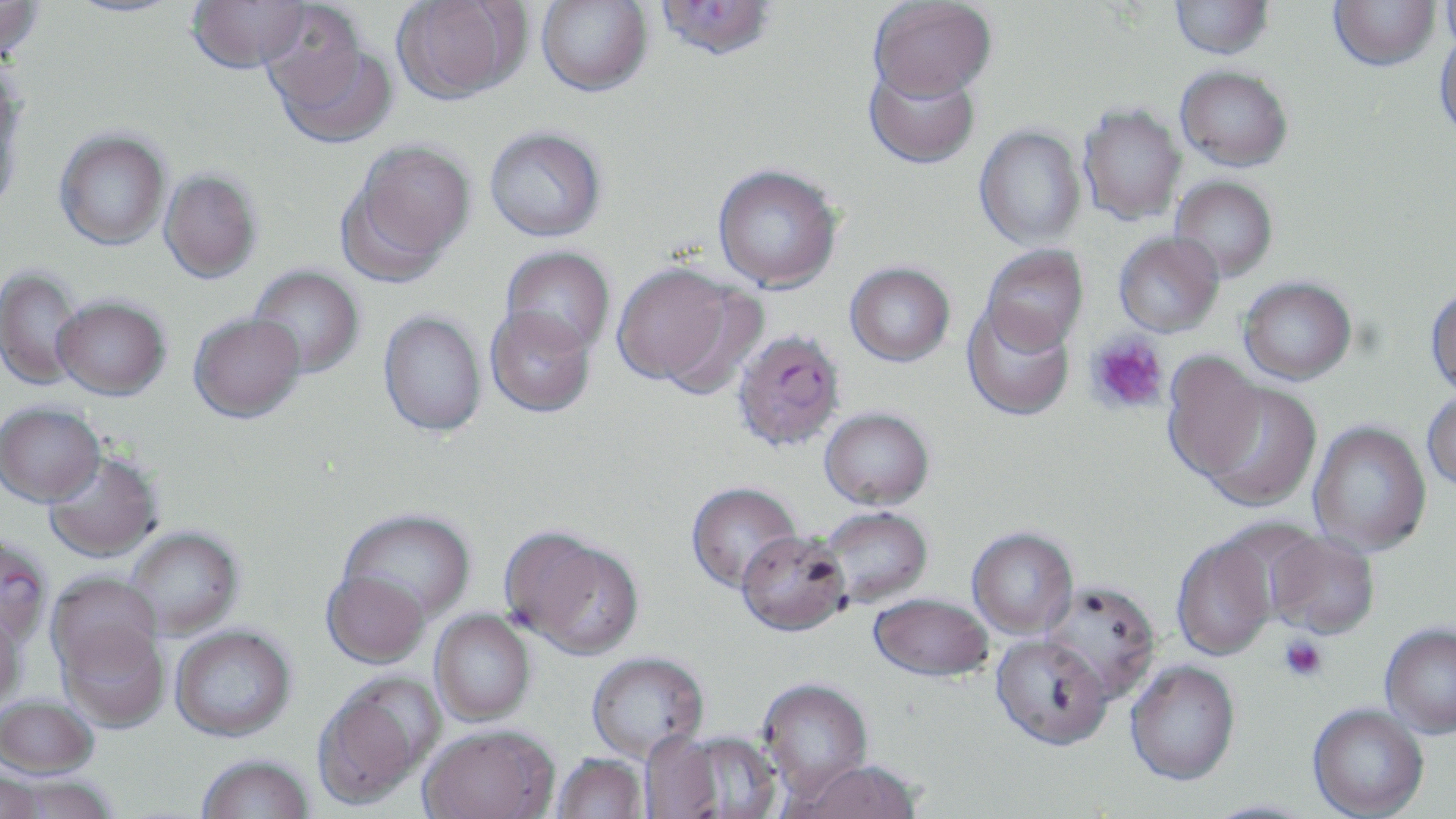

Summary:
  - Coordinate format: approximate bounding boxes as named x1/y1/x2/y2 corners in pixels
  - Platelet locations: (x1=1087, y1=331, x2=1169, y2=415), (x1=1279, y1=635, x2=1328, y2=681)
  - Uninfected red blood cell locations: (x1=0, y1=0, x2=45, y2=62), (x1=61, y1=0, x2=186, y2=18), (x1=186, y1=0, x2=311, y2=74), (x1=391, y1=0, x2=529, y2=105), (x1=535, y1=0, x2=653, y2=97), (x1=1330, y1=0, x2=1440, y2=71), (x1=654, y1=1, x2=777, y2=62), (x1=869, y1=1, x2=996, y2=102), (x1=1169, y1=1, x2=1273, y2=59), (x1=1440, y1=1, x2=1456, y2=56), (x1=262, y1=10, x2=396, y2=149), (x1=1434, y1=28, x2=1456, y2=142), (x1=863, y1=58, x2=981, y2=170), (x1=1175, y1=65, x2=1293, y2=171), (x1=0, y1=95, x2=23, y2=217), (x1=1078, y1=104, x2=1185, y2=224), (x1=974, y1=125, x2=1086, y2=249), (x1=485, y1=126, x2=607, y2=242), (x1=54, y1=129, x2=171, y2=250), (x1=339, y1=140, x2=476, y2=283), (x1=712, y1=163, x2=843, y2=292), (x1=159, y1=170, x2=262, y2=283), (x1=1170, y1=175, x2=1278, y2=282), (x1=1114, y1=231, x2=1224, y2=337), (x1=980, y1=245, x2=1088, y2=354), (x1=500, y1=246, x2=615, y2=357), (x1=611, y1=262, x2=749, y2=391), (x1=844, y1=262, x2=955, y2=366), (x1=247, y1=265, x2=364, y2=379), (x1=0, y1=266, x2=85, y2=391), (x1=1239, y1=276, x2=1357, y2=384), (x1=1425, y1=285, x2=1456, y2=397), (x1=53, y1=295, x2=171, y2=399), (x1=961, y1=302, x2=1075, y2=421), (x1=485, y1=307, x2=596, y2=418), (x1=378, y1=310, x2=487, y2=438), (x1=188, y1=313, x2=306, y2=423), (x1=1162, y1=352, x2=1269, y2=483), (x1=1198, y1=381, x2=1322, y2=511), (x1=1421, y1=388, x2=1456, y2=492), (x1=0, y1=401, x2=106, y2=506), (x1=819, y1=407, x2=935, y2=510), (x1=1308, y1=421, x2=1431, y2=557), (x1=43, y1=451, x2=163, y2=562), (x1=685, y1=481, x2=803, y2=592), (x1=818, y1=506, x2=933, y2=607), (x1=337, y1=508, x2=476, y2=624), (x1=124, y1=526, x2=244, y2=639), (x1=967, y1=527, x2=1078, y2=638), (x1=505, y1=529, x2=645, y2=659), (x1=736, y1=530, x2=851, y2=636), (x1=1263, y1=530, x2=1380, y2=640), (x1=1171, y1=533, x2=1281, y2=662), (x1=321, y1=569, x2=430, y2=669), (x1=48, y1=572, x2=163, y2=680), (x1=1039, y1=581, x2=1162, y2=703), (x1=869, y1=593, x2=994, y2=684), (x1=0, y1=606, x2=27, y2=711), (x1=430, y1=609, x2=535, y2=726), (x1=59, y1=619, x2=170, y2=731), (x1=170, y1=624, x2=296, y2=742), (x1=1380, y1=625, x2=1456, y2=740), (x1=990, y1=636, x2=1112, y2=754), (x1=586, y1=651, x2=708, y2=762), (x1=1125, y1=662, x2=1240, y2=789), (x1=312, y1=675, x2=440, y2=811), (x1=757, y1=679, x2=874, y2=799), (x1=0, y1=695, x2=99, y2=779), (x1=1307, y1=706, x2=1428, y2=819), (x1=418, y1=724, x2=559, y2=819), (x1=660, y1=730, x2=782, y2=819), (x1=551, y1=753, x2=649, y2=819), (x1=196, y1=754, x2=316, y2=818), (x1=783, y1=761, x2=924, y2=819), (x1=0, y1=768, x2=46, y2=819), (x1=2, y1=774, x2=120, y2=819), (x1=1201, y1=799, x2=1321, y2=819)
  - Plasmodium falciparum-infected red blood cell locations: (x1=732, y1=328, x2=847, y2=453), (x1=0, y1=533, x2=53, y2=646)
  - Slide-level diagnosis: Plasmodium falciparum
  - Magnification: 1000x
  - Field of view: one of a larger specimen
  - Stain: May-Grünwald-Giemsa
  - Modality: optical microscopy
  - Image size: 1456×819 pixels
  - Preparation: thin blood smear